Assess this cell for malaria.
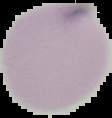

Uninfected.

image_size: 112×118 pixels
image_type: segmented cell region on a black background
preparation: thin blood smear